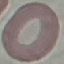

result = negative for malaria parasites
stain = Giemsa
preparation = thin blood smear
capture = smartphone camera at the microscope eyepiece
image type = automatically extracted cell patch, resized to 64 × 64 pixels